State which parasite is depicted.
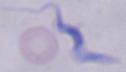

This is a trypanosome.

1000x magnification. Micrograph.